Assess this cell for malaria.
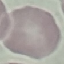
Uninfected.

Summary:
  - Stain: Giemsa
  - Capture: smartphone through the microscope eyepiece
  - Image type: automatically extracted cell patch, resized to 64 × 64 pixels
  - Preparation: thin blood film